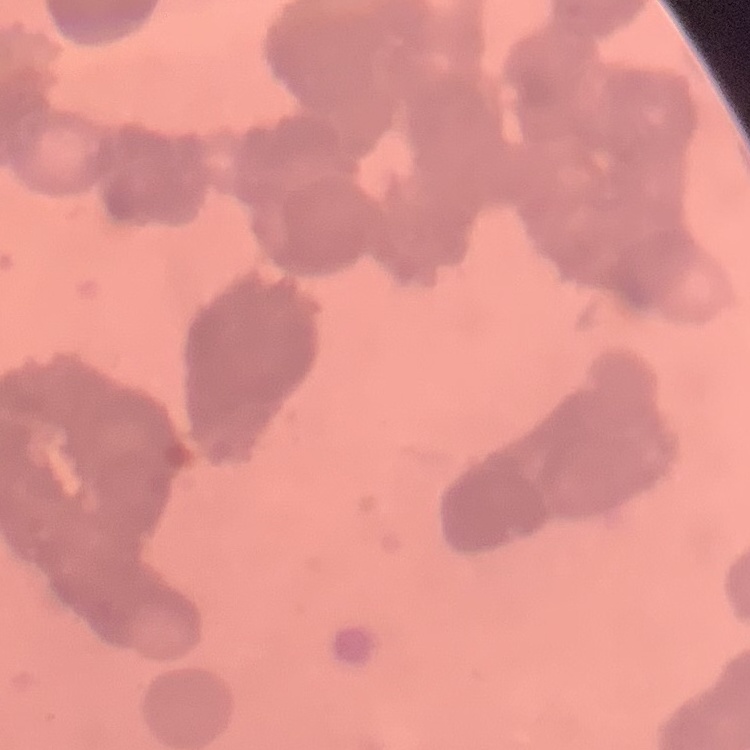
The red blood cells exhibit rouleaux formation. Thin peripheral smear. Square crop of a larger photomicrograph. Field's or Giemsa stain.